Report the malaria status of this cell.
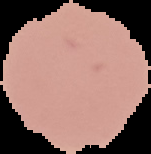
It is uninfected.

{
  "image_type": "segmented cell region with the area outside set to black",
  "preparation": "thin blood film",
  "image_size": "151×154 pixels"
}